State the blood parasite species.
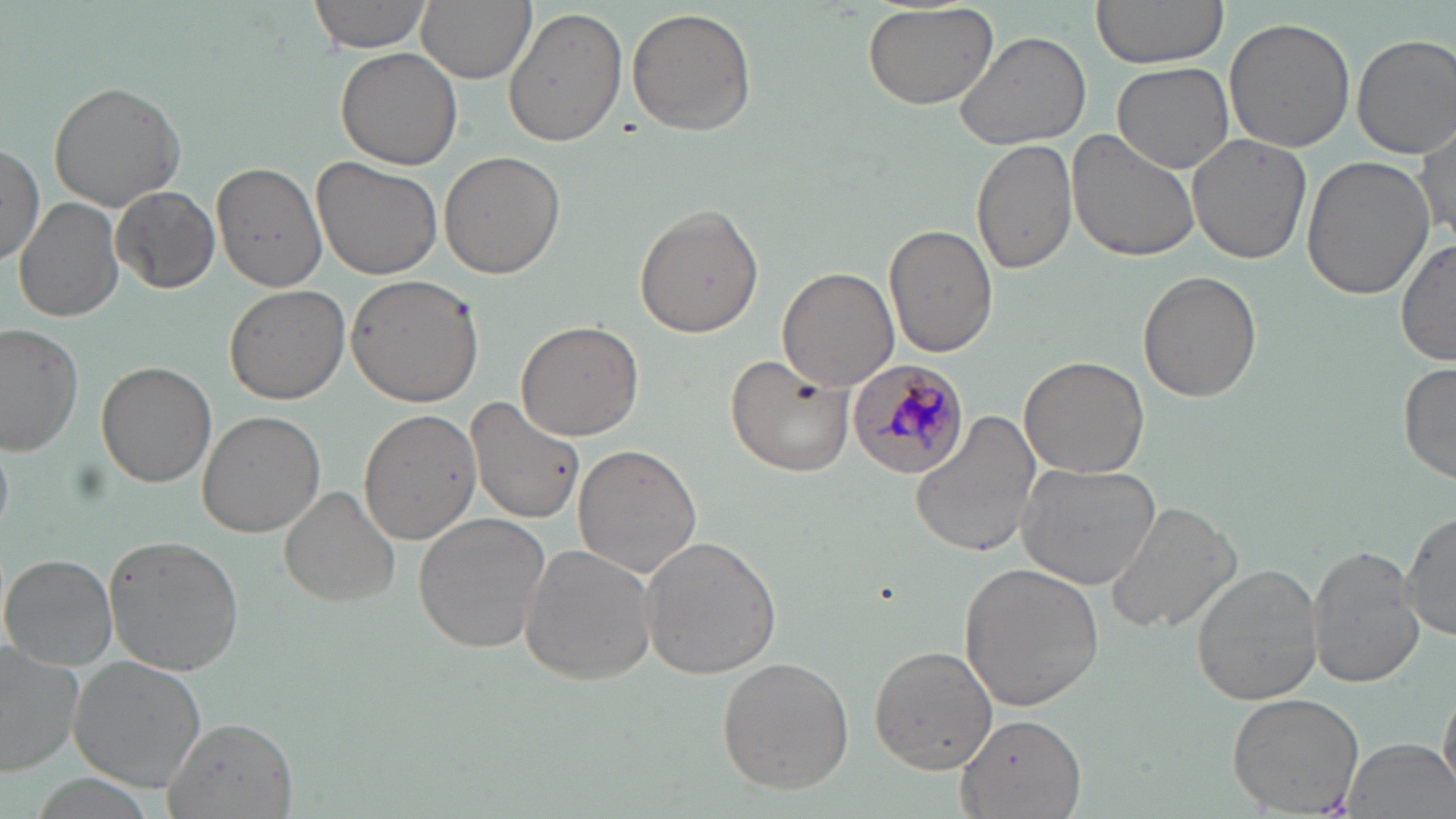

Plasmodium malariae.

magnification = 1000x
modality = optical microscopy
stain = May-Grünwald-Giemsa
image size = 1456×819 pixels
field of view = one of a larger specimen
uninfected red blood cell locations = approximate bounding boxes as named x1/y1/x2/y2 corners in pixels: (x1=308, y1=0, x2=437, y2=56), (x1=417, y1=0, x2=534, y2=83), (x1=1089, y1=0, x2=1229, y2=70), (x1=863, y1=2, x2=1000, y2=111), (x1=504, y1=7, x2=628, y2=147), (x1=627, y1=7, x2=757, y2=137), (x1=1224, y1=17, x2=1355, y2=153), (x1=954, y1=29, x2=1095, y2=151), (x1=1352, y1=33, x2=1456, y2=158), (x1=336, y1=46, x2=463, y2=171), (x1=1111, y1=61, x2=1236, y2=174), (x1=48, y1=78, x2=188, y2=212), (x1=1415, y1=118, x2=1454, y2=241), (x1=1067, y1=128, x2=1204, y2=263), (x1=1186, y1=133, x2=1312, y2=265), (x1=972, y1=137, x2=1078, y2=274), (x1=0, y1=142, x2=45, y2=266), (x1=439, y1=150, x2=564, y2=279), (x1=1302, y1=156, x2=1433, y2=300), (x1=313, y1=159, x2=441, y2=281), (x1=213, y1=161, x2=326, y2=292), (x1=109, y1=185, x2=221, y2=294), (x1=14, y1=198, x2=124, y2=325), (x1=634, y1=205, x2=765, y2=338), (x1=883, y1=222, x2=998, y2=357), (x1=1396, y1=237, x2=1456, y2=367), (x1=777, y1=266, x2=900, y2=392), (x1=1139, y1=272, x2=1261, y2=403), (x1=346, y1=273, x2=484, y2=407), (x1=223, y1=284, x2=350, y2=405), (x1=516, y1=320, x2=643, y2=440), (x1=1, y1=322, x2=84, y2=455), (x1=725, y1=355, x2=854, y2=477), (x1=1021, y1=355, x2=1149, y2=477), (x1=97, y1=360, x2=217, y2=487), (x1=1398, y1=361, x2=1456, y2=482), (x1=463, y1=395, x2=584, y2=524), (x1=354, y1=406, x2=487, y2=545), (x1=198, y1=410, x2=324, y2=537), (x1=909, y1=410, x2=1043, y2=559), (x1=0, y1=441, x2=14, y2=530), (x1=574, y1=444, x2=704, y2=578), (x1=1017, y1=460, x2=1164, y2=589), (x1=278, y1=485, x2=401, y2=609), (x1=1105, y1=498, x2=1239, y2=633), (x1=413, y1=512, x2=553, y2=652), (x1=1399, y1=513, x2=1455, y2=641), (x1=103, y1=534, x2=244, y2=675), (x1=638, y1=534, x2=782, y2=681), (x1=521, y1=543, x2=659, y2=684), (x1=1308, y1=546, x2=1424, y2=689), (x1=2, y1=554, x2=119, y2=670), (x1=957, y1=563, x2=1104, y2=709), (x1=1190, y1=564, x2=1324, y2=704), (x1=0, y1=643, x2=83, y2=779), (x1=868, y1=645, x2=997, y2=773), (x1=69, y1=655, x2=209, y2=791), (x1=717, y1=655, x2=855, y2=794), (x1=1439, y1=675, x2=1456, y2=800), (x1=1227, y1=691, x2=1366, y2=815), (x1=957, y1=713, x2=1087, y2=817), (x1=166, y1=714, x2=296, y2=817), (x1=1340, y1=736, x2=1455, y2=819)
Plasmodium malariae-infected red blood cell locations = approximate bounding boxes as named x1/y1/x2/y2 corners in pixels: (x1=842, y1=360, x2=965, y2=480)
preparation = thin blood smear